State which cell type is depicted.
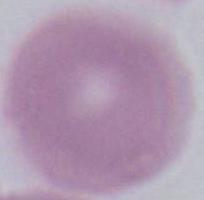
An erythrocyte.

Captured at 1000x magnification. Photomicrograph.